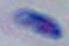
modality = photomicrograph
magnification = 1000x
identification = Toxoplasma gondii